Locate the Plasmodium falciparum-infected red blood cells and any of indeterminate infection status.
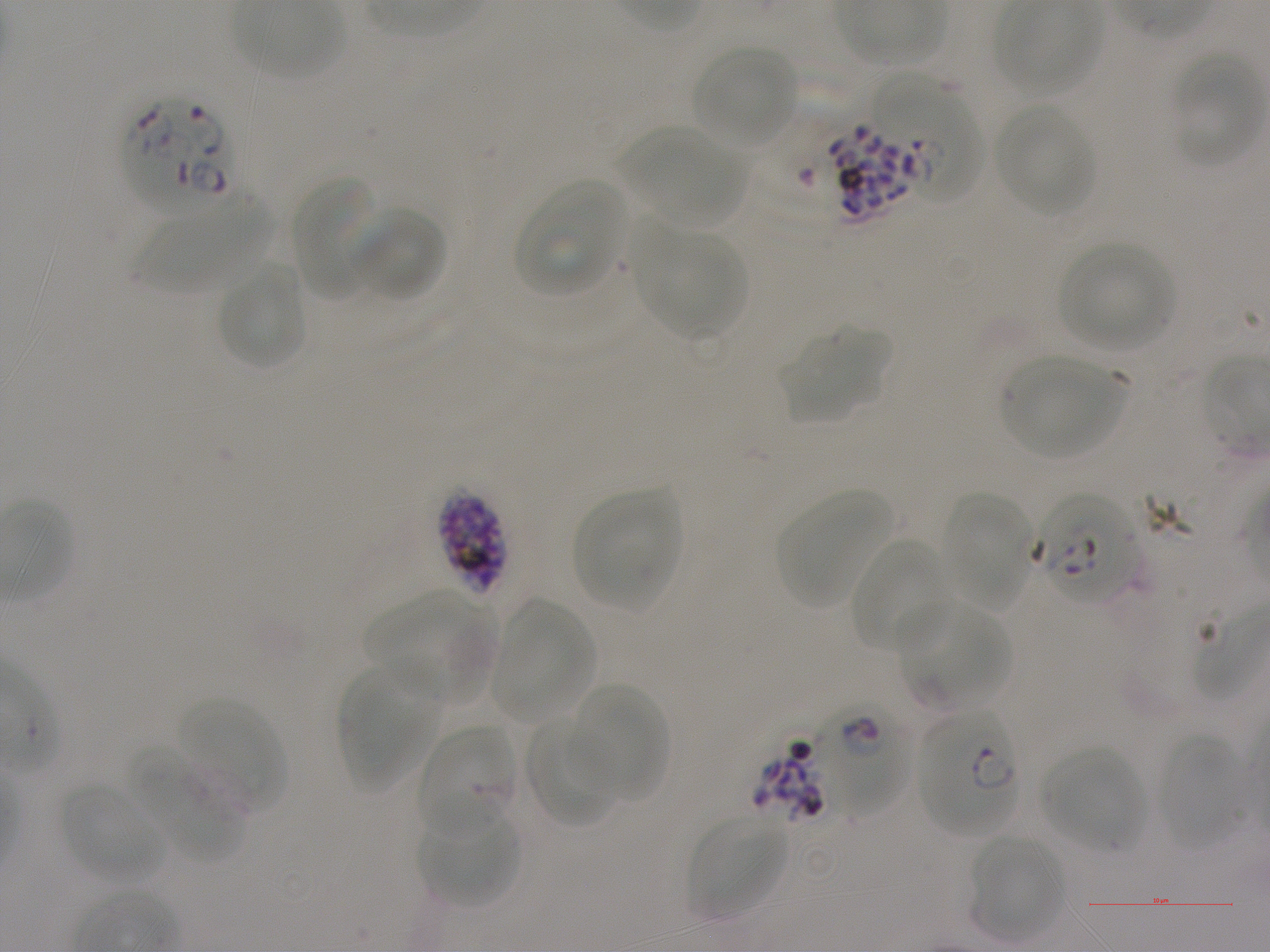

Approximate bounding boxes as [x1, y1, x2, y2] in pixels. Not every red blood cell is marked. A life-cycle stage — or a range of stages, where the recorded stages span more than one — follows each staged infected red blood cell.
Infected red blood cells: [125, 96, 241, 213]; [828, 122, 929, 221] late schizont; [437, 489, 509, 596] late schizont; [1034, 489, 1140, 609]; [813, 700, 907, 816]; [918, 710, 1019, 834] ring.
Red blood cells of indeterminate infection status: [899, 94, 995, 215], [419, 726, 519, 839], [751, 738, 827, 823].

{
  "locations_of_uninfected_red_blood_cells": "[692, 45, 798, 148], [1170, 56, 1261, 165], [871, 72, 957, 145], [995, 102, 1096, 216], [631, 131, 746, 228], [291, 176, 381, 299], [514, 179, 626, 297], [136, 184, 276, 292], [350, 205, 446, 304], [640, 228, 745, 338], [1059, 242, 1174, 350], [217, 265, 306, 369], [779, 326, 889, 423], [1001, 357, 1127, 459], [573, 489, 681, 610], [774, 489, 895, 608], [940, 493, 1033, 609], [849, 538, 951, 653], [366, 590, 495, 703], [493, 599, 594, 724], [900, 602, 1006, 708], [336, 661, 440, 788], [572, 684, 670, 802], [180, 699, 284, 805], [524, 716, 619, 827], [1156, 732, 1245, 848], [1041, 746, 1149, 853], [131, 749, 246, 860], [61, 784, 165, 883], [418, 806, 520, 908], [688, 814, 787, 917], [968, 834, 1065, 939]",
  "life_cycle_stages_observed": "ring, schizont",
  "field_of_view": "one from this slide",
  "culture": "static in-vitro Plasmodium falciparum strain NF54",
  "objective": "100x, oil immersion, numerical aperture 1.25",
  "donor_blood_group": "A+",
  "preparation": "thin blood film",
  "image_size": "1270×952 pixels",
  "stain": "Giemsa"
}